Name the parasite shown.
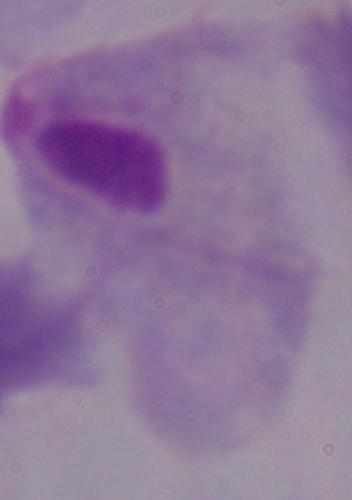

A trichomonad.

Micrograph. 1000x magnification.